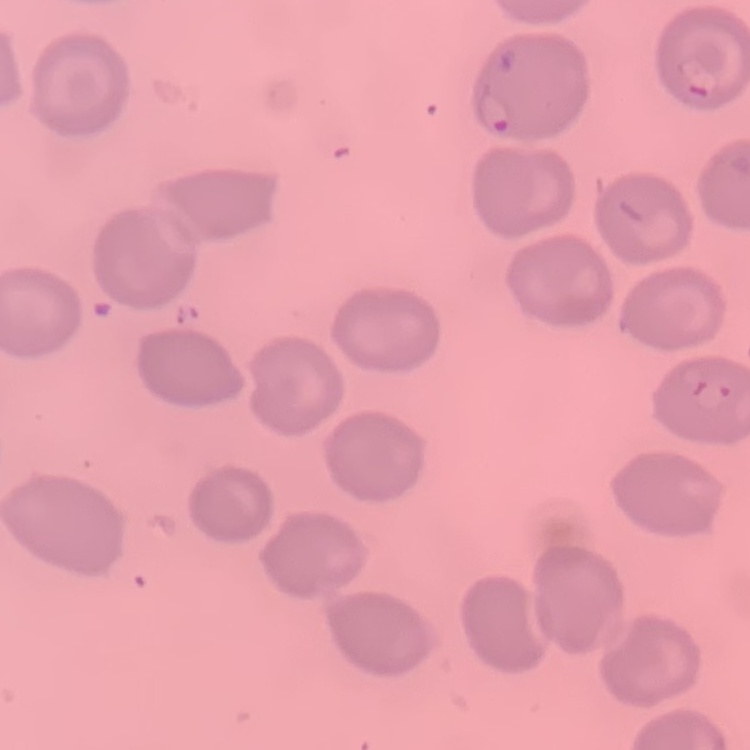

{
  "erythrocyte_morphology": "no rouleaux formation",
  "stain": "Field's or Giemsa",
  "preparation": "thin blood film",
  "image_type": "square crop of a larger photomicrograph"
}